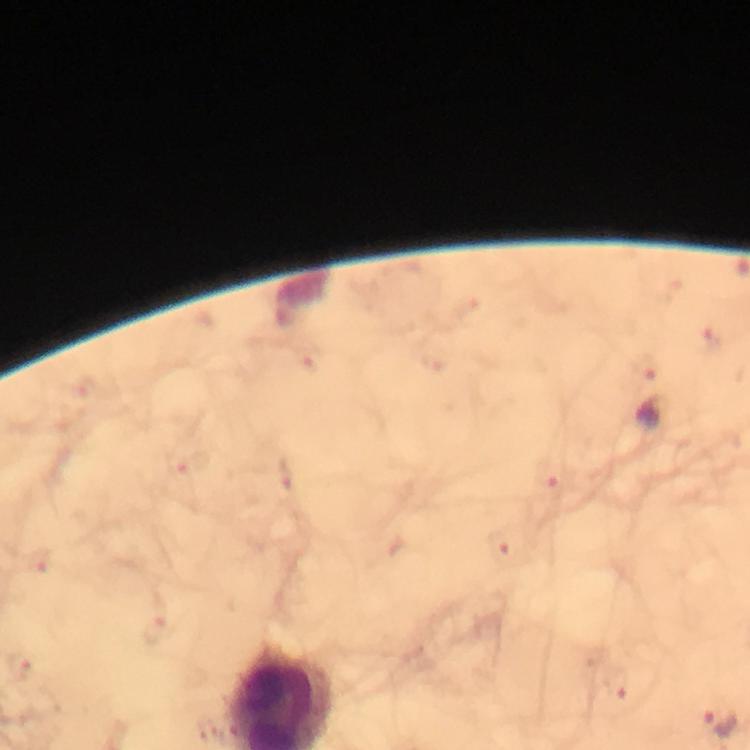

Approximate centers as {x, y} in pixels.
Summary:
  - Plasmodium parasite locations: {711, 338}, {648, 365}, {552, 476}, {501, 546}, {40, 561}, {157, 629}, {21, 666}, {616, 685}, {720, 723}
  - Magnification: 100x
  - Immersion oil: applied
  - Cropped from: a single field of view
  - Context: from a diagnostic examination for malaria
  - Stain: Giemsa
  - Capture: smartphone photograph through a microscope
  - Image size: 750×750 pixels
  - Preparation: thick blood film